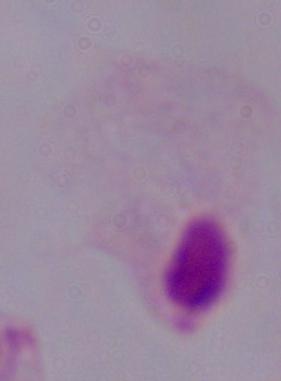

Summary:
  - Modality: micrograph
  - Magnification: 1000x
  - Identification: trichomonad